Report the malaria status of this cell.
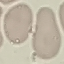
Uninfected.

Summary:
  - Stain: Giemsa
  - Capture: smartphone camera at the microscope eyepiece
  - Preparation: thin blood film
  - Image type: cell patch, automatically extracted from a larger field of view and resized to 64 × 64 pixels